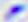 Photomicrograph. 400x magnification. Toxoplasma gondii is shown.